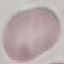

malaria_status: uninfected
image_type: cell patch, automatically extracted from a larger field of view and resized to 64 × 64 pixels
stain: Giemsa
preparation: thin blood film
capture: smartphone through the microscope eyepiece